Identify the parasite.
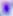

This is Toxoplasma gondii.

magnification = 400x
modality = photomicrograph